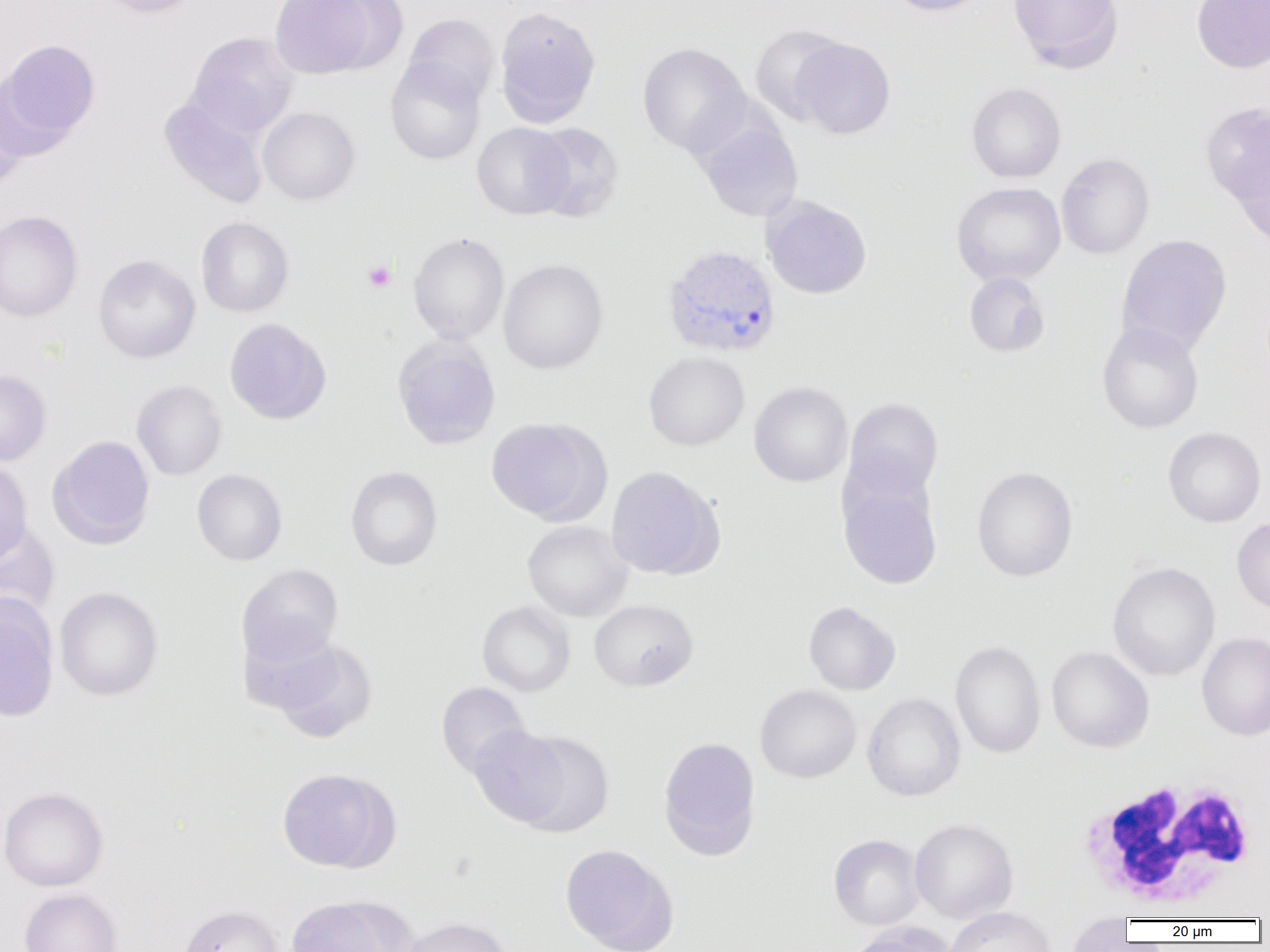
Summary:
  - Coordinate format: approximate bounding boxes as named x1/y1/x2/y2 corners in pixels
  - Uninfected red blood cell locations: (x1=96, y1=0, x2=206, y2=18), (x1=270, y1=0, x2=380, y2=78), (x1=319, y1=0, x2=408, y2=75), (x1=883, y1=0, x2=990, y2=16), (x1=1008, y1=0, x2=1124, y2=72), (x1=1191, y1=0, x2=1270, y2=73), (x1=495, y1=7, x2=601, y2=127), (x1=403, y1=14, x2=499, y2=106), (x1=749, y1=23, x2=849, y2=126), (x1=187, y1=32, x2=297, y2=138), (x1=793, y1=38, x2=895, y2=139), (x1=0, y1=39, x2=100, y2=153), (x1=638, y1=42, x2=751, y2=157), (x1=385, y1=56, x2=486, y2=165), (x1=966, y1=83, x2=1066, y2=182), (x1=0, y1=88, x2=27, y2=193), (x1=159, y1=96, x2=269, y2=209), (x1=1200, y1=101, x2=1270, y2=206), (x1=258, y1=107, x2=360, y2=205), (x1=697, y1=119, x2=803, y2=221), (x1=472, y1=122, x2=573, y2=219), (x1=529, y1=123, x2=624, y2=222), (x1=1232, y1=149, x2=1270, y2=252), (x1=1056, y1=153, x2=1155, y2=259), (x1=951, y1=182, x2=1065, y2=286), (x1=763, y1=197, x2=872, y2=299), (x1=0, y1=210, x2=83, y2=322), (x1=196, y1=217, x2=293, y2=317), (x1=408, y1=232, x2=509, y2=346), (x1=1116, y1=234, x2=1232, y2=355), (x1=93, y1=255, x2=200, y2=363), (x1=498, y1=259, x2=608, y2=374), (x1=964, y1=272, x2=1051, y2=357), (x1=224, y1=318, x2=331, y2=424), (x1=1097, y1=321, x2=1204, y2=434), (x1=392, y1=337, x2=501, y2=449), (x1=644, y1=352, x2=749, y2=451), (x1=0, y1=370, x2=51, y2=466), (x1=132, y1=380, x2=227, y2=480), (x1=749, y1=382, x2=852, y2=487), (x1=843, y1=398, x2=944, y2=500), (x1=485, y1=416, x2=606, y2=525), (x1=1163, y1=427, x2=1266, y2=527), (x1=47, y1=435, x2=155, y2=550), (x1=0, y1=459, x2=33, y2=564), (x1=345, y1=466, x2=442, y2=571), (x1=606, y1=466, x2=723, y2=579), (x1=972, y1=466, x2=1078, y2=582), (x1=192, y1=469, x2=287, y2=566), (x1=838, y1=475, x2=942, y2=590), (x1=1232, y1=517, x2=1270, y2=614), (x1=522, y1=520, x2=632, y2=622), (x1=0, y1=522, x2=60, y2=624), (x1=1107, y1=561, x2=1220, y2=681), (x1=236, y1=564, x2=344, y2=668), (x1=54, y1=586, x2=163, y2=701), (x1=0, y1=596, x2=59, y2=722), (x1=589, y1=599, x2=699, y2=692), (x1=477, y1=601, x2=575, y2=696), (x1=803, y1=601, x2=901, y2=695), (x1=239, y1=624, x2=341, y2=715), (x1=1197, y1=632, x2=1270, y2=741), (x1=272, y1=640, x2=377, y2=743), (x1=950, y1=640, x2=1046, y2=759), (x1=1046, y1=646, x2=1154, y2=752), (x1=436, y1=682, x2=531, y2=778), (x1=755, y1=685, x2=862, y2=783), (x1=862, y1=692, x2=965, y2=801), (x1=468, y1=724, x2=572, y2=827), (x1=514, y1=731, x2=615, y2=837), (x1=658, y1=736, x2=762, y2=860), (x1=276, y1=768, x2=394, y2=872), (x1=0, y1=787, x2=108, y2=891), (x1=910, y1=818, x2=1018, y2=923), (x1=829, y1=834, x2=924, y2=930), (x1=560, y1=844, x2=678, y2=951), (x1=18, y1=888, x2=123, y2=952), (x1=287, y1=897, x2=396, y2=952), (x1=177, y1=904, x2=283, y2=952), (x1=943, y1=906, x2=1057, y2=952), (x1=1066, y1=913, x2=1134, y2=952), (x1=398, y1=917, x2=512, y2=952), (x1=848, y1=922, x2=956, y2=952)
  - Plasmodium vivax-infected red blood cell locations: (x1=662, y1=245, x2=781, y2=358)
  - White blood cell locations: (x1=1076, y1=777, x2=1261, y2=913)
  - Platelet locations: (x1=362, y1=260, x2=397, y2=292)
  - Slide-level diagnosis: Plasmodium vivax
  - Magnification: 1000x
  - Preparation: thin blood smear
  - Modality: light microscopy
  - Field of view: one of a larger specimen
  - Image size: 1270×952 pixels